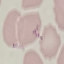
malaria_status: uninfected
preparation: thin blood smear
stain: Giemsa
image_type: cell patch, automatically extracted from a larger field of view and resized to 64 × 64 pixels
capture: smartphone through the microscope eyepiece